State which parasite is depicted.
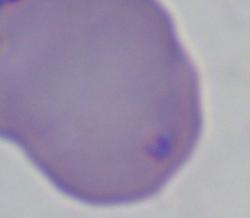

This is Babesia.

Summary:
  - Magnification: 1000x
  - Modality: photomicrograph